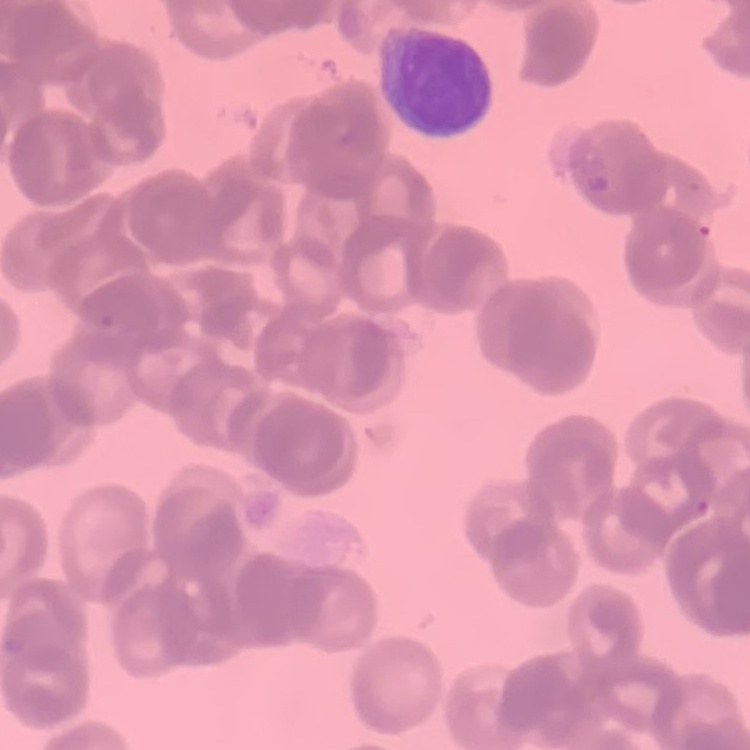
The red blood cells show rouleaux formation. Square crop of a larger photomicrograph. Thin peripheral smear. Field's or Giemsa stain.